State the blood parasite species.
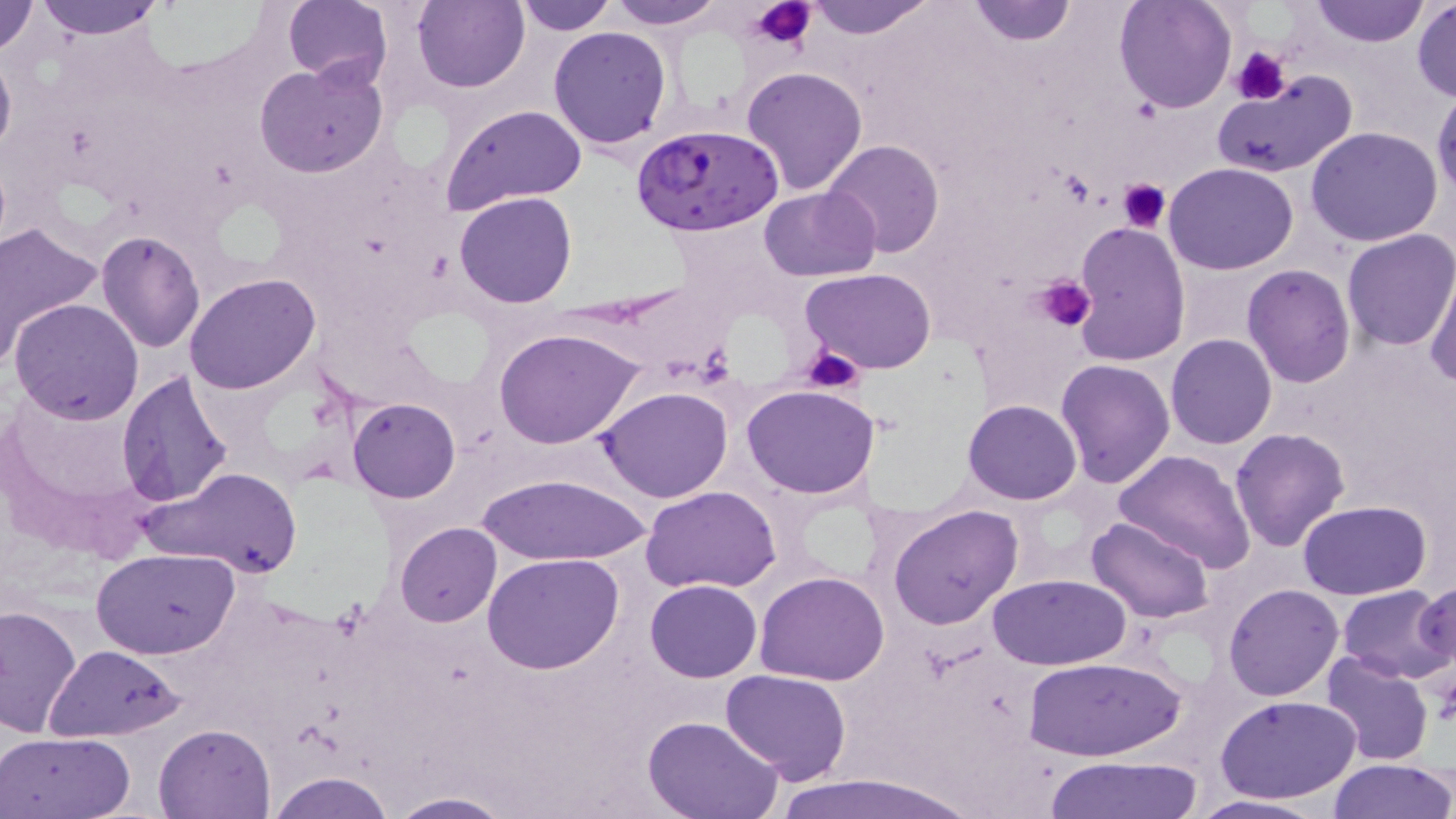

Plasmodium falciparum.

Approximate bounding boxes as named x1/y1/x2/y2 corners in pixels. Plasmodium falciparum-infected red blood cell locations: (x1=630, y1=123, x2=785, y2=237). Platelet locations: (x1=748, y1=0, x2=816, y2=50), (x1=1233, y1=48, x2=1290, y2=103), (x1=1117, y1=177, x2=1173, y2=231), (x1=1036, y1=276, x2=1097, y2=333), (x1=804, y1=346, x2=864, y2=395). Uninfected red blood cell locations: (x1=0, y1=0, x2=41, y2=57), (x1=31, y1=0, x2=169, y2=39), (x1=412, y1=0, x2=530, y2=93), (x1=515, y1=0, x2=617, y2=34), (x1=603, y1=0, x2=728, y2=30), (x1=806, y1=0, x2=936, y2=39), (x1=966, y1=0, x2=1076, y2=45), (x1=1115, y1=0, x2=1236, y2=114), (x1=1310, y1=0, x2=1428, y2=47), (x1=283, y1=1, x2=393, y2=90), (x1=1411, y1=1, x2=1455, y2=103), (x1=549, y1=26, x2=671, y2=151), (x1=0, y1=42, x2=15, y2=163), (x1=255, y1=60, x2=389, y2=178), (x1=741, y1=65, x2=868, y2=195), (x1=1212, y1=70, x2=1357, y2=180), (x1=1432, y1=88, x2=1456, y2=203), (x1=441, y1=103, x2=588, y2=213), (x1=1305, y1=126, x2=1443, y2=246), (x1=823, y1=139, x2=945, y2=256), (x1=1163, y1=163, x2=1298, y2=276), (x1=758, y1=185, x2=880, y2=281), (x1=454, y1=192, x2=578, y2=308), (x1=1073, y1=220, x2=1190, y2=366), (x1=0, y1=221, x2=104, y2=361), (x1=1341, y1=228, x2=1455, y2=352), (x1=96, y1=229, x2=205, y2=352), (x1=1241, y1=264, x2=1356, y2=388), (x1=799, y1=269, x2=939, y2=375), (x1=1425, y1=271, x2=1456, y2=389), (x1=185, y1=274, x2=319, y2=394), (x1=9, y1=297, x2=144, y2=425), (x1=494, y1=327, x2=643, y2=448), (x1=1165, y1=333, x2=1277, y2=450), (x1=1056, y1=358, x2=1176, y2=488), (x1=116, y1=369, x2=234, y2=508), (x1=743, y1=384, x2=876, y2=498), (x1=597, y1=386, x2=733, y2=501), (x1=348, y1=397, x2=461, y2=503), (x1=963, y1=399, x2=1082, y2=504), (x1=1228, y1=427, x2=1349, y2=551), (x1=1114, y1=450, x2=1257, y2=573), (x1=145, y1=465, x2=303, y2=580), (x1=477, y1=472, x2=653, y2=565), (x1=643, y1=485, x2=782, y2=594), (x1=1299, y1=501, x2=1430, y2=600), (x1=888, y1=504, x2=1024, y2=629), (x1=1087, y1=515, x2=1215, y2=622), (x1=394, y1=522, x2=501, y2=627), (x1=91, y1=549, x2=241, y2=659), (x1=483, y1=554, x2=625, y2=675), (x1=755, y1=570, x2=889, y2=685), (x1=986, y1=573, x2=1131, y2=669), (x1=646, y1=580, x2=761, y2=682), (x1=1416, y1=580, x2=1455, y2=679), (x1=1223, y1=583, x2=1343, y2=701), (x1=1336, y1=584, x2=1454, y2=683), (x1=0, y1=604, x2=83, y2=738), (x1=43, y1=643, x2=187, y2=742), (x1=1320, y1=652, x2=1435, y2=766), (x1=1026, y1=654, x2=1185, y2=762), (x1=720, y1=669, x2=850, y2=784), (x1=1219, y1=695, x2=1361, y2=804), (x1=643, y1=716, x2=784, y2=819), (x1=153, y1=722, x2=277, y2=817), (x1=0, y1=734, x2=136, y2=819), (x1=1045, y1=756, x2=1205, y2=818), (x1=1329, y1=758, x2=1455, y2=818), (x1=266, y1=772, x2=398, y2=819), (x1=762, y1=772, x2=982, y2=819), (x1=384, y1=792, x2=514, y2=819), (x1=1186, y1=794, x2=1332, y2=818). One field of a larger specimen. Light microscopy. Thin blood smear. May-Grünwald-Giemsa stain. Captured at 1000x magnification. Image is 1456×819 pixels.